Look for parasitized red blood cells.
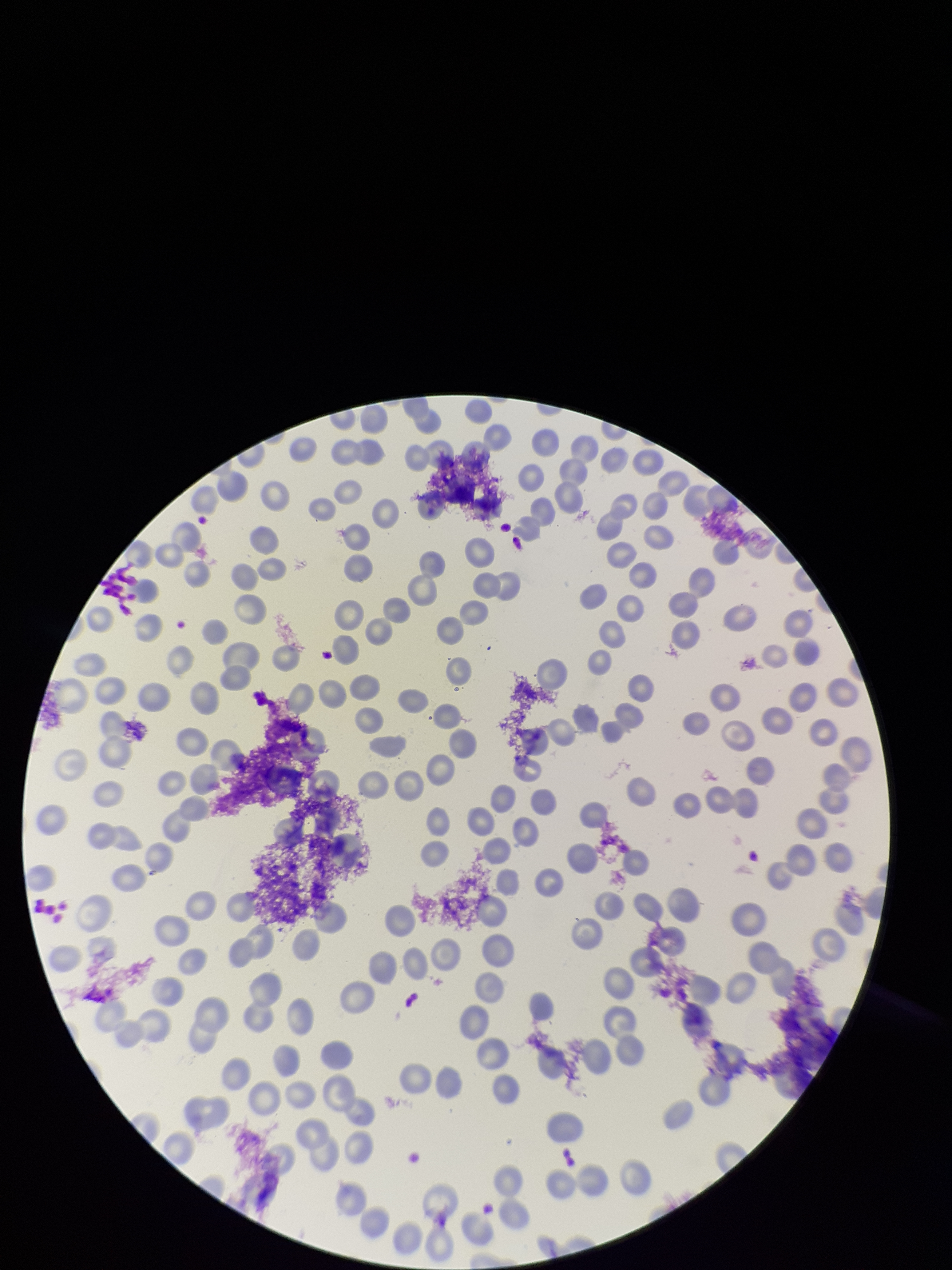
None detected.

image size = 952×1270 pixels
field of view = one from this slide
red blood cell count = 185
patient malaria status = negative
capture = smartphone photograph through the microscope eyepiece
preparation = thin blood smear
stain = Giemsa
parasitized red blood cell count = 0